Locate every Plasmodium parasite.
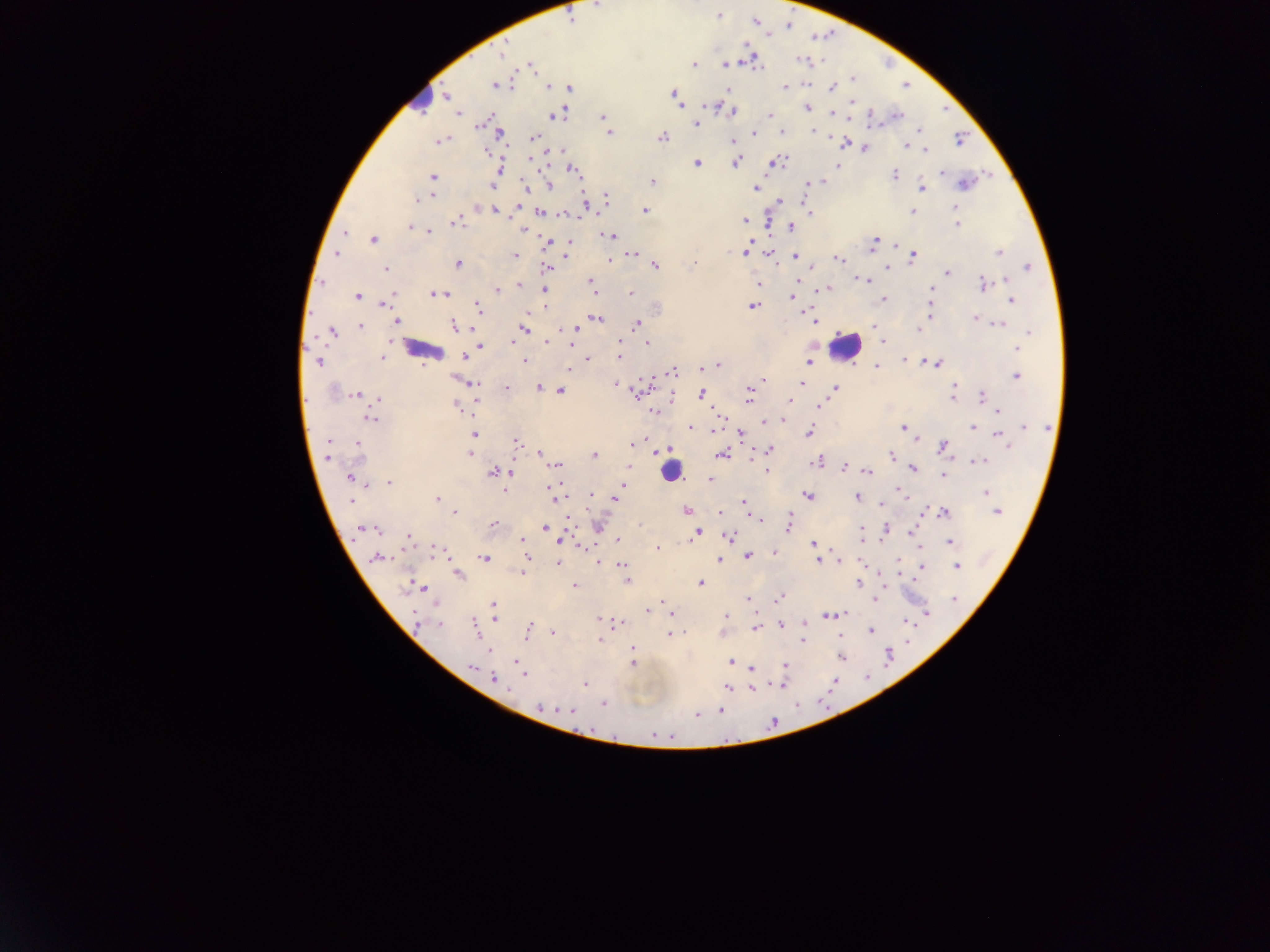
Approximate centers as {x, y} in pixels.
Plasmodium parasites: {717, 16}, {755, 21}, {788, 25}, {502, 53}, {753, 59}, {803, 60}, {693, 64}, {725, 64}, {531, 66}, {852, 79}, {494, 86}, {548, 86}, {785, 87}, {832, 87}, {569, 88}, {728, 89}, {673, 95}, {446, 96}, {677, 102}, {853, 102}, {807, 108}, {833, 111}, {732, 112}, {459, 114}, {556, 115}, {770, 115}, {896, 115}, {603, 116}, {482, 125}, {696, 125}, {813, 131}, {608, 132}, {781, 132}, {754, 133}, {500, 135}, {534, 137}, {663, 137}, {960, 139}, {734, 141}, {439, 142}, {845, 143}, {906, 146}, {865, 148}, {925, 150}, {486, 152}, {736, 162}, {775, 162}, {697, 163}, {837, 165}, {573, 170}, {498, 171}, {942, 173}, {894, 175}, {432, 176}, {821, 181}, {652, 182}, {964, 183}, {808, 185}, {549, 186}, {493, 187}, {525, 188}, {922, 188}, {756, 189}, {431, 195}, {607, 200}, {416, 201}, {585, 206}, {495, 210}, {646, 211}, {912, 211}, {956, 211}, {541, 213}, {564, 213}, {810, 213}, {744, 221}, {456, 223}, {956, 224}, {409, 226}, {791, 227}, {524, 231}, {429, 232}, {344, 233}, {611, 235}, {373, 240}, {548, 242}, {569, 242}, {874, 243}, {744, 252}, {770, 252}, {998, 252}, {336, 255}, {515, 255}, {567, 255}, {631, 255}, {796, 256}, {913, 257}, {609, 259}, {838, 259}, {694, 263}, {458, 264}, {655, 266}, {1028, 266}, {546, 267}, {887, 267}, {386, 268}, {948, 271}, {590, 280}, {797, 281}, {864, 281}, {1006, 281}, {758, 283}, {983, 284}, {520, 285}, {544, 288}, {498, 289}, {827, 289}, {932, 289}, {630, 293}, {393, 294}, {433, 294}, {444, 294}, {358, 296}, {791, 297}, {883, 299}, {389, 300}, {1013, 300}, {384, 304}, {751, 306}, {544, 307}, {477, 309}, {539, 309}, {931, 310}, {975, 317}, {596, 318}, {813, 320}, {396, 322}, {636, 324}, {999, 324}, {454, 325}, {359, 326}, {873, 326}, {523, 329}, {574, 329}, {918, 330}, {332, 332}, {1028, 332}, {546, 341}, {513, 342}, {883, 342}, {620, 343}, {648, 343}, {480, 346}, {571, 346}, {1017, 349}, {471, 354}, {619, 356}, {383, 357}, {464, 357}, {588, 359}, {526, 361}, {905, 361}, {318, 362}, {809, 362}, {936, 364}, {716, 365}, {709, 366}, {876, 367}, {569, 370}, {673, 371}, {1016, 376}, {764, 379}, {802, 383}, {474, 384}, {616, 385}, {955, 386}, {538, 387}, {507, 388}, {835, 388}, {559, 390}, {636, 391}, {750, 392}, {700, 394}, {356, 395}, {954, 396}, {982, 397}, {377, 399}, {748, 400}, {791, 400}, {820, 405}, {456, 406}, {654, 411}, {998, 411}, {369, 419}, {782, 420}, {764, 421}, {1024, 426}, {691, 427}, {974, 427}, {902, 428}, {809, 432}, {473, 435}, {741, 435}, {999, 436}, {917, 439}, {516, 442}, {328, 443}, {1006, 443}, {633, 444}, {356, 445}, {944, 446}, {770, 450}, {663, 452}, {469, 453}, {540, 454}, {722, 454}, {595, 455}, {327, 456}, {890, 456}, {817, 461}, {979, 462}, {558, 465}, {629, 466}, {844, 468}, {913, 468}, {767, 471}, {868, 472}, {494, 473}, {510, 473}, {943, 476}, {350, 477}, {709, 480}, {388, 482}, {623, 484}, {504, 490}, {553, 490}, {899, 491}, {986, 493}, {591, 495}, {905, 495}, {808, 496}, {857, 496}, {555, 497}, {438, 498}, {616, 499}, {351, 501}, {744, 502}, {881, 505}, {687, 510}, {944, 512}, {997, 512}, {454, 513}, {719, 513}, {759, 520}, {790, 523}, {492, 525}, {546, 527}, {364, 529}, {886, 530}, {376, 531}, {863, 532}, {697, 533}, {912, 533}, {729, 537}, {409, 538}, {861, 538}, {618, 540}, {522, 541}, {563, 541}, {950, 542}, {814, 543}, {657, 547}, {436, 552}, {773, 552}, {722, 556}, {749, 556}, {527, 557}, {378, 558}, {485, 558}, {720, 559}, {598, 560}, {818, 560}, {839, 561}, {557, 563}, {623, 565}, {957, 566}, {921, 567}, {522, 572}, {458, 575}, {628, 582}, {700, 583}, {858, 584}, {573, 585}, {411, 586}, {421, 587}, {779, 597}, {749, 599}, {876, 599}, {956, 600}, {661, 603}, {494, 605}, {647, 611}, {670, 612}, {926, 612}, {840, 613}, {827, 615}, {495, 616}, {725, 616}, {415, 618}, {598, 619}, {617, 623}, {439, 625}, {781, 626}, {476, 628}, {755, 628}, {527, 632}, {553, 632}, {870, 632}, {670, 635}, {599, 639}, {803, 639}, {632, 649}, {887, 656}, {841, 658}, {517, 662}, {731, 662}, {633, 663}, {785, 666}, {472, 667}, {752, 668}, {525, 674}, {494, 678}, {585, 684}, {780, 684}, {727, 687}, {752, 688}, {603, 704}, {541, 708}, {572, 710}, {720, 711}, {697, 715}, {654, 735}.

Summary:
  - Leukocyte locations: {422, 95}, {844, 344}, {665, 473}
  - Capture: mobile-phone photograph through a microscope
  - Field of view: single
  - Country: Ghana
  - Image size: 1270×952 pixels
  - Preparation: thick blood smear